Point out each malaria parasite and each leukocyte.
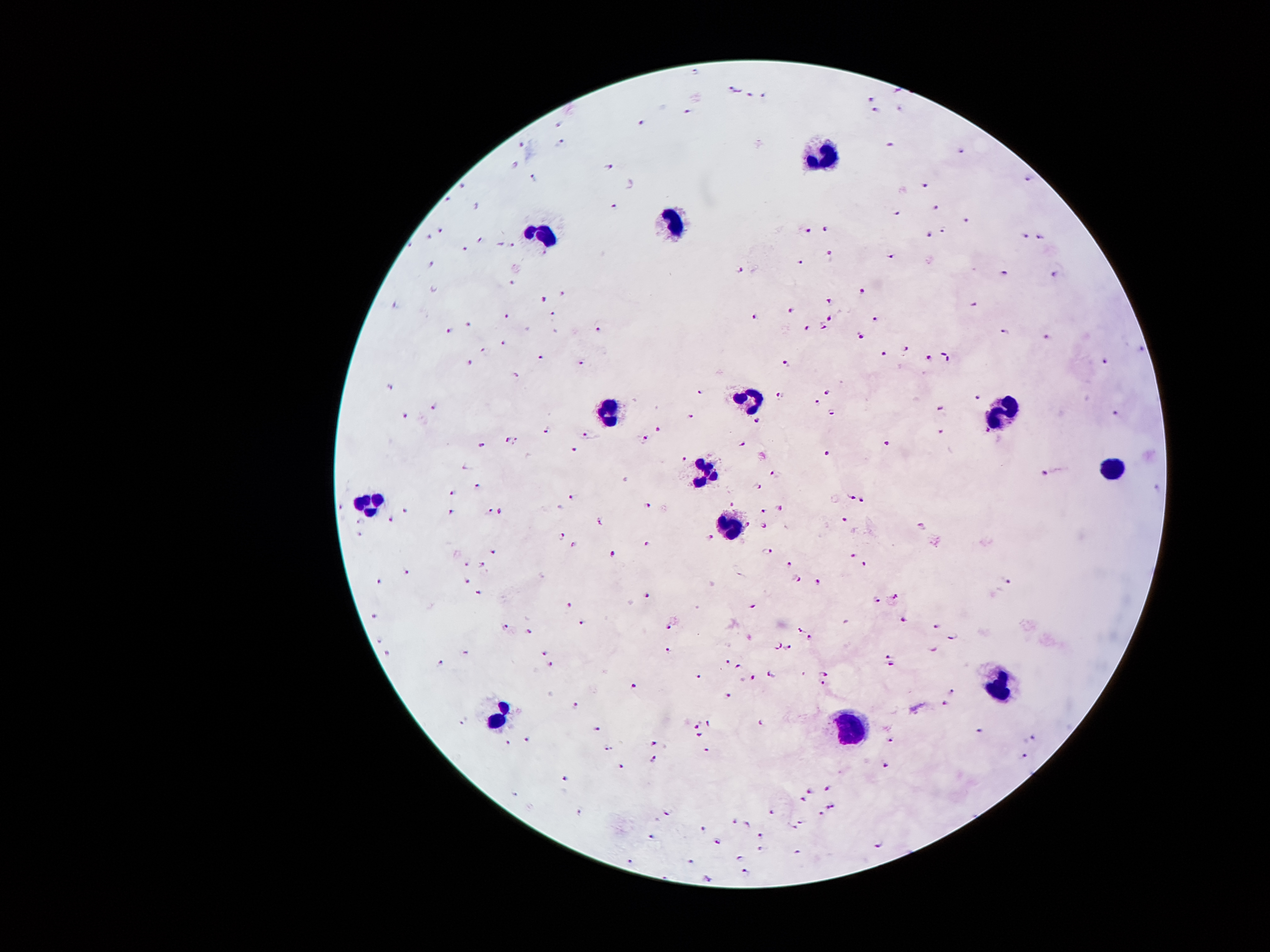

Approximate object centers, in pixels from the top-left corner.
Malaria parasites: (x=693, y=73), (x=734, y=89), (x=761, y=92), (x=745, y=96), (x=871, y=100), (x=895, y=110), (x=686, y=113), (x=875, y=114), (x=558, y=122), (x=638, y=122), (x=522, y=143), (x=559, y=145), (x=891, y=146), (x=961, y=154), (x=513, y=166), (x=607, y=168), (x=1024, y=178), (x=531, y=180), (x=924, y=183), (x=462, y=189), (x=449, y=199), (x=611, y=206), (x=932, y=209), (x=898, y=214), (x=967, y=220), (x=827, y=229), (x=810, y=230), (x=944, y=231), (x=438, y=233), (x=929, y=234), (x=1024, y=235), (x=429, y=238), (x=1039, y=238), (x=477, y=241), (x=510, y=245), (x=463, y=248), (x=829, y=255), (x=892, y=256), (x=800, y=262), (x=428, y=265), (x=740, y=269), (x=1005, y=275), (x=1054, y=276), (x=510, y=282), (x=861, y=291), (x=561, y=294), (x=544, y=300), (x=827, y=301), (x=393, y=307), (x=791, y=310), (x=551, y=314), (x=506, y=317), (x=752, y=318), (x=829, y=318), (x=875, y=318), (x=470, y=324), (x=821, y=327), (x=600, y=329), (x=802, y=330), (x=449, y=331), (x=1005, y=332), (x=858, y=335), (x=1046, y=335), (x=502, y=343), (x=907, y=349), (x=481, y=353), (x=883, y=355), (x=541, y=356), (x=926, y=358), (x=468, y=363), (x=789, y=363), (x=1105, y=363), (x=580, y=364), (x=518, y=373), (x=389, y=390), (x=827, y=390), (x=699, y=391), (x=779, y=397), (x=978, y=397), (x=816, y=402), (x=437, y=406), (x=938, y=407), (x=1117, y=412), (x=833, y=414), (x=691, y=415), (x=408, y=417), (x=757, y=423), (x=659, y=430), (x=986, y=430), (x=940, y=432), (x=543, y=433), (x=588, y=433), (x=512, y=440), (x=643, y=441), (x=888, y=444), (x=740, y=445), (x=481, y=446), (x=572, y=449), (x=824, y=454), (x=685, y=460), (x=1046, y=473), (x=774, y=474), (x=474, y=486), (x=758, y=487), (x=454, y=493), (x=849, y=497), (x=569, y=498), (x=732, y=502), (x=860, y=503), (x=648, y=504), (x=342, y=507), (x=488, y=508), (x=781, y=509), (x=408, y=512), (x=453, y=512), (x=500, y=512), (x=762, y=512), (x=843, y=519), (x=363, y=520), (x=391, y=521), (x=600, y=523), (x=747, y=524), (x=762, y=528), (x=924, y=528), (x=357, y=535), (x=711, y=538), (x=563, y=539), (x=575, y=546), (x=646, y=547), (x=493, y=550), (x=769, y=552), (x=611, y=553), (x=853, y=556), (x=789, y=564), (x=471, y=565), (x=483, y=567), (x=866, y=567), (x=404, y=573), (x=464, y=579), (x=797, y=580), (x=819, y=582), (x=378, y=583), (x=1007, y=585), (x=477, y=592), (x=644, y=595), (x=894, y=597), (x=874, y=600), (x=571, y=604), (x=751, y=606), (x=372, y=617), (x=904, y=621), (x=581, y=622), (x=505, y=626), (x=669, y=627), (x=937, y=627), (x=799, y=632), (x=529, y=633), (x=376, y=638), (x=953, y=638), (x=814, y=639), (x=787, y=646), (x=779, y=647), (x=934, y=647), (x=668, y=651), (x=467, y=653), (x=387, y=655), (x=546, y=655), (x=884, y=656), (x=437, y=664), (x=726, y=664), (x=740, y=665), (x=891, y=665), (x=550, y=666), (x=770, y=675), (x=825, y=675), (x=699, y=678), (x=752, y=678), (x=821, y=683), (x=634, y=686), (x=951, y=690), (x=728, y=696), (x=945, y=703), (x=576, y=705), (x=466, y=721), (x=765, y=721), (x=709, y=723), (x=695, y=727), (x=597, y=728), (x=978, y=733), (x=697, y=736), (x=526, y=739), (x=1030, y=740), (x=653, y=742), (x=891, y=742), (x=508, y=743), (x=607, y=749), (x=705, y=751), (x=1021, y=757), (x=652, y=759), (x=886, y=765), (x=621, y=768), (x=564, y=781), (x=828, y=788), (x=810, y=789), (x=803, y=797), (x=831, y=806), (x=580, y=812), (x=668, y=812), (x=769, y=814), (x=820, y=816), (x=803, y=821), (x=735, y=823), (x=745, y=825), (x=701, y=828), (x=794, y=829), (x=651, y=835), (x=762, y=835), (x=716, y=842), (x=881, y=844), (x=760, y=850), (x=798, y=854), (x=739, y=857), (x=691, y=860), (x=630, y=861), (x=744, y=871), (x=706, y=877).
Leukocytes: (x=824, y=158), (x=669, y=222), (x=548, y=236), (x=750, y=398), (x=999, y=412), (x=609, y=415), (x=1110, y=469), (x=703, y=473), (x=733, y=474), (x=370, y=503), (x=732, y=527), (x=996, y=683), (x=500, y=717), (x=851, y=732).

Image is 1270×952 pixels. Giemsa stain. 100x magnification. Patient malaria status: positive for Plasmodium falciparum. Thick blood smear. Smartphone photograph taken through the microscope eyepiece. One field from this slide.